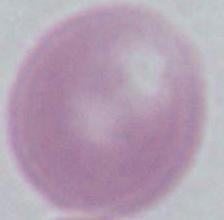
{
  "magnification": "1000x",
  "identification": "red blood cell",
  "modality": "micrograph"
}